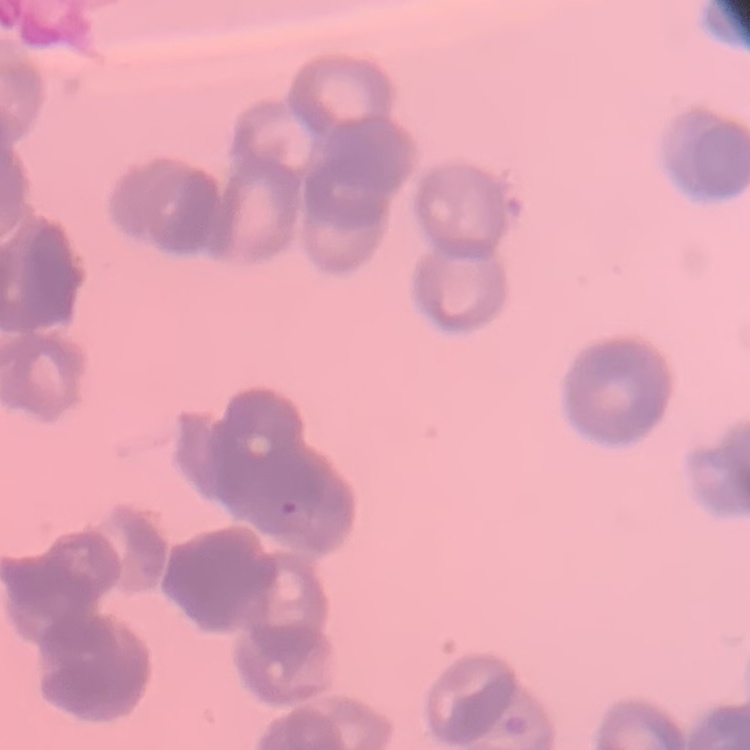

red blood cell morphology = rouleaux formation
preparation = thin blood film
image type = one tile cut from a larger photomicrograph
stain = Field's or Giemsa